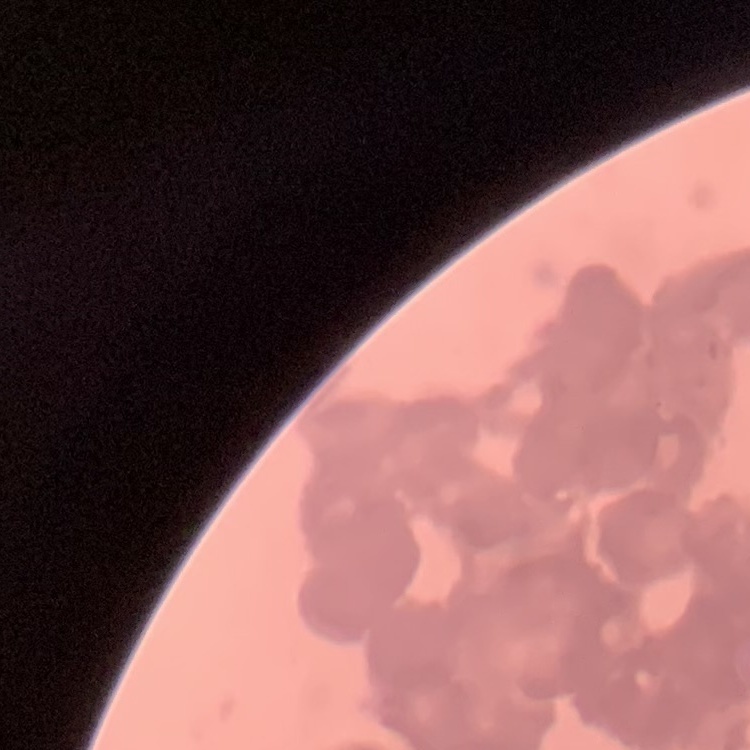

erythrocyte_morphology: rouleaux formation
stain: Field's or Giemsa
preparation: thin peripheral smear
image_type: one tile cut from a larger photomicrograph